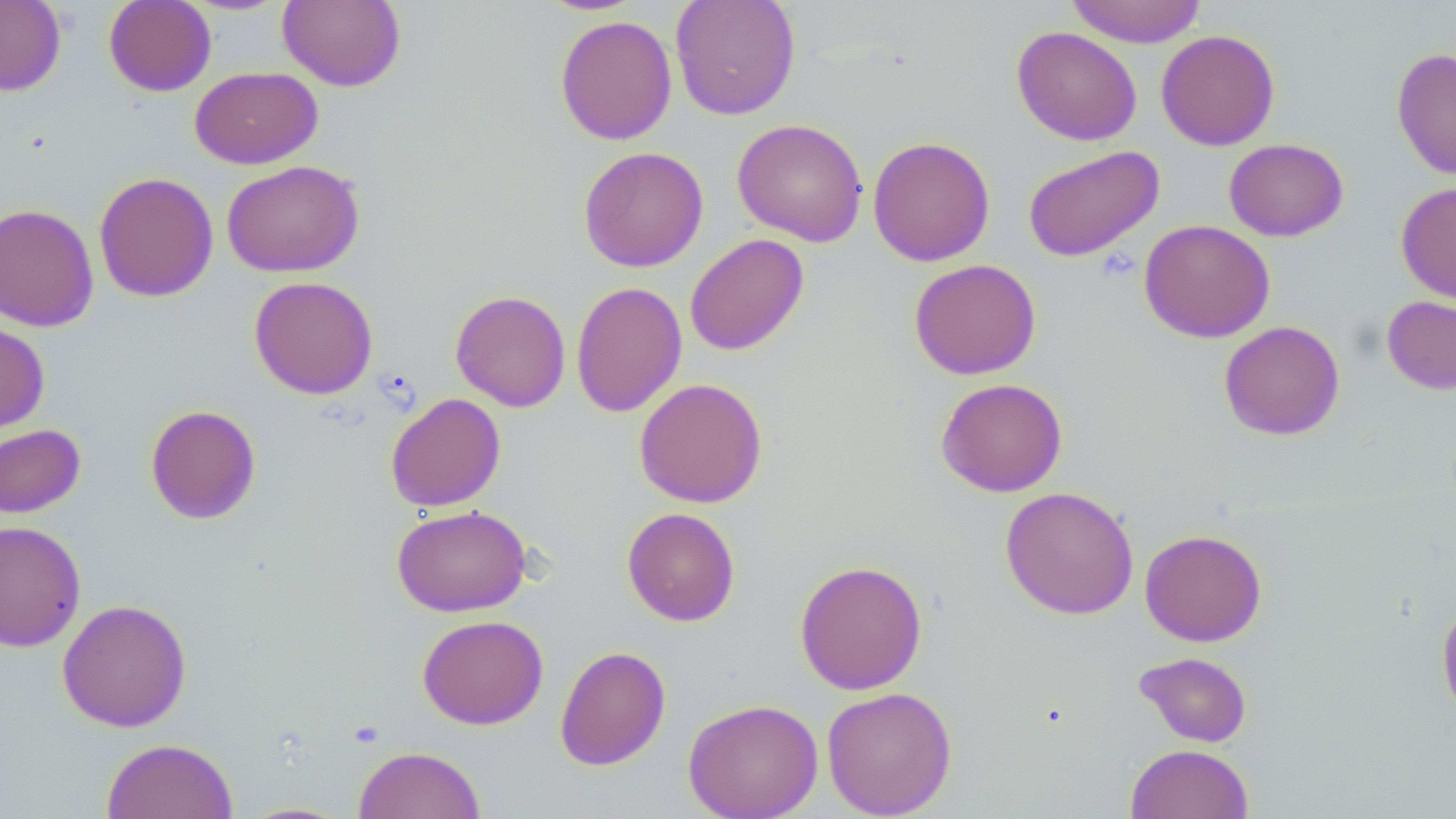
Summary:
  - Coordinate format: approximate bounding boxes as (x1,y1)-(x2,y2) corner pairs in pixels
  - Uninfected red blood cell locations: (0,0)-(66,96), (104,0)-(216,96), (670,0)-(801,120), (1065,0)-(1207,47), (277,1)-(406,92), (554,14)-(677,145), (1011,26)-(1142,145), (1156,29)-(1280,151), (1391,47)-(1456,179), (190,66)-(323,169), (732,118)-(867,246), (867,136)-(995,267), (1224,138)-(1348,241), (1022,145)-(1165,262), (578,146)-(709,272), (221,159)-(365,278), (94,172)-(218,302), (1396,181)-(1456,304), (0,203)-(99,332), (1138,219)-(1276,343), (684,234)-(809,356), (908,259)-(1041,380), (249,276)-(378,399), (571,282)-(687,417), (450,289)-(571,412), (1381,295)-(1456,395), (0,320)-(50,435), (1218,320)-(1345,441), (935,377)-(1067,497), (634,378)-(768,508), (385,393)-(506,512), (145,404)-(262,525), (0,424)-(86,518), (1000,486)-(1139,620), (391,504)-(532,616), (622,507)-(741,626), (0,520)-(86,652), (1140,528)-(1267,647), (794,559)-(928,695), (1436,596)-(1456,723), (57,599)-(192,732), (417,614)-(548,730), (554,645)-(671,771), (1135,651)-(1252,747), (821,686)-(957,818), (682,698)-(823,819), (100,738)-(237,819), (1125,743)-(1254,819), (353,745)-(485,819)
  - Slide-level diagnosis: no evidence of blood parasites
  - Preparation: thin blood smear
  - Image size: 1456×819 pixels
  - Field of view: single
  - Magnification: 1000x
  - Stain: May-Grünwald-Giemsa
  - Modality: light microscopy